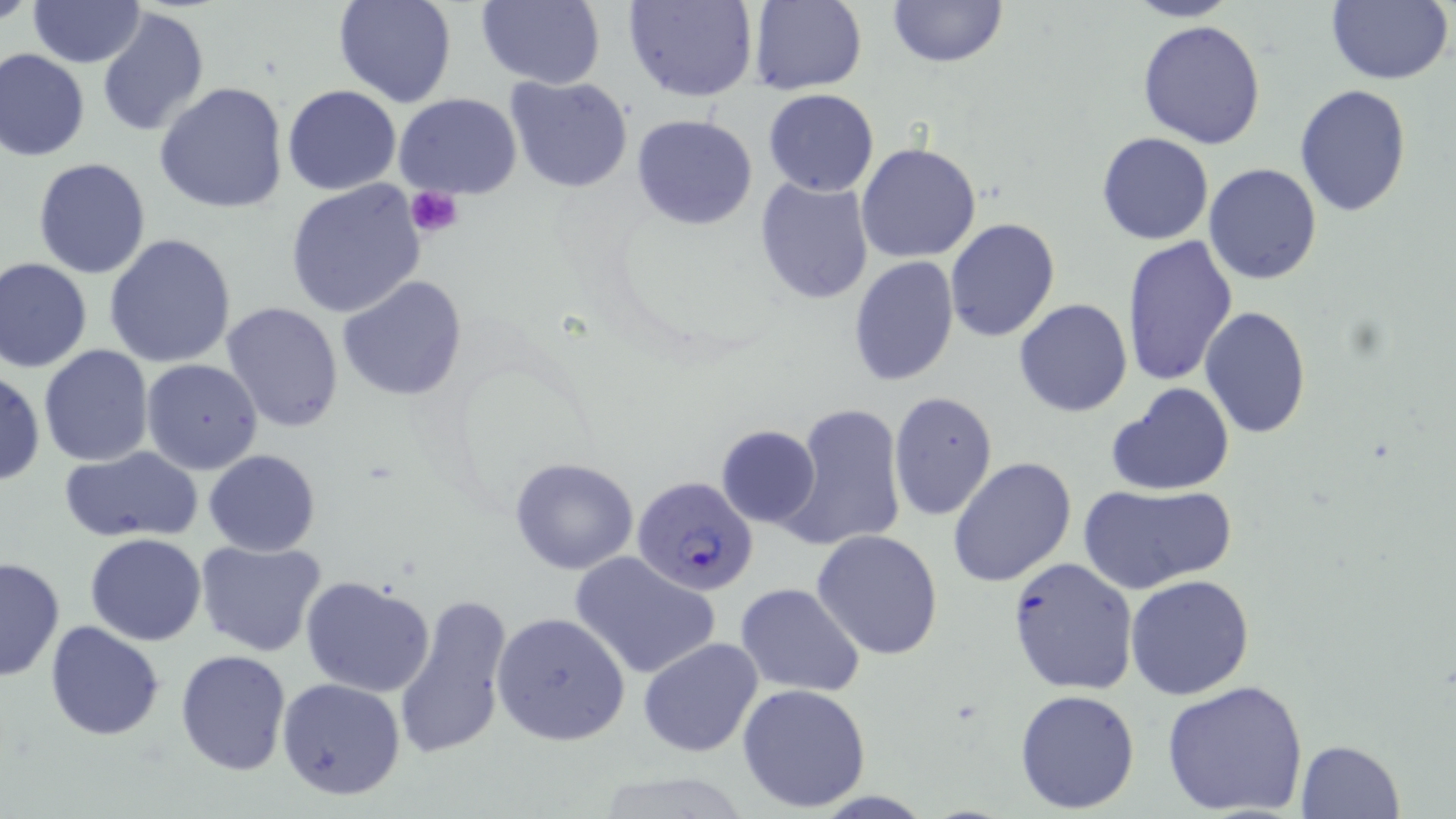

Summary:
  - Coordinate format: approximate bounding boxes as named x1/y1/x2/y2 corners in pixels
  - Plasmodium falciparum-infected red blood cell locations: (x1=633, y1=475, x2=760, y2=595)
  - Uninfected red blood cell locations: (x1=0, y1=0, x2=37, y2=28), (x1=26, y1=0, x2=145, y2=67), (x1=332, y1=0, x2=456, y2=109), (x1=475, y1=0, x2=604, y2=88), (x1=625, y1=0, x2=757, y2=102), (x1=888, y1=0, x2=1006, y2=68), (x1=1123, y1=0, x2=1243, y2=22), (x1=1327, y1=0, x2=1454, y2=85), (x1=750, y1=1, x2=868, y2=95), (x1=97, y1=7, x2=210, y2=138), (x1=1137, y1=19, x2=1268, y2=150), (x1=1, y1=48, x2=90, y2=162), (x1=506, y1=75, x2=633, y2=193), (x1=154, y1=81, x2=290, y2=216), (x1=1295, y1=84, x2=1412, y2=216), (x1=282, y1=85, x2=402, y2=195), (x1=763, y1=89, x2=880, y2=196), (x1=395, y1=93, x2=522, y2=200), (x1=631, y1=112, x2=759, y2=230), (x1=1097, y1=131, x2=1213, y2=245), (x1=855, y1=140, x2=982, y2=263), (x1=33, y1=157, x2=153, y2=279), (x1=1204, y1=163, x2=1321, y2=284), (x1=754, y1=177, x2=873, y2=305), (x1=284, y1=180, x2=428, y2=321), (x1=944, y1=217, x2=1060, y2=342), (x1=103, y1=233, x2=237, y2=369), (x1=1121, y1=233, x2=1238, y2=386), (x1=0, y1=256, x2=93, y2=373), (x1=848, y1=257, x2=960, y2=388), (x1=337, y1=276, x2=467, y2=399), (x1=1014, y1=299, x2=1134, y2=417), (x1=221, y1=301, x2=344, y2=433), (x1=1199, y1=308, x2=1311, y2=438), (x1=39, y1=346, x2=154, y2=466), (x1=141, y1=358, x2=265, y2=475), (x1=0, y1=368, x2=43, y2=489), (x1=1107, y1=383, x2=1236, y2=497), (x1=888, y1=390, x2=997, y2=523), (x1=781, y1=403, x2=905, y2=553), (x1=715, y1=425, x2=821, y2=529), (x1=60, y1=447, x2=204, y2=544), (x1=204, y1=449, x2=320, y2=556), (x1=508, y1=456, x2=638, y2=574), (x1=948, y1=457, x2=1077, y2=589), (x1=1079, y1=483, x2=1235, y2=592), (x1=1019, y1=517, x2=1174, y2=663), (x1=810, y1=529, x2=943, y2=662), (x1=84, y1=533, x2=208, y2=644), (x1=195, y1=539, x2=329, y2=657), (x1=570, y1=550, x2=723, y2=680), (x1=0, y1=555, x2=64, y2=682), (x1=1007, y1=557, x2=1139, y2=696), (x1=1124, y1=574, x2=1254, y2=700), (x1=300, y1=575, x2=437, y2=697), (x1=736, y1=583, x2=865, y2=698), (x1=394, y1=594, x2=513, y2=760), (x1=492, y1=610, x2=631, y2=745), (x1=45, y1=620, x2=164, y2=739), (x1=637, y1=636, x2=765, y2=756), (x1=174, y1=649, x2=291, y2=776), (x1=277, y1=677, x2=407, y2=800), (x1=1163, y1=678, x2=1309, y2=818), (x1=737, y1=683, x2=872, y2=812), (x1=1014, y1=688, x2=1142, y2=814), (x1=1296, y1=739, x2=1406, y2=819)
  - Platelet locations: (x1=406, y1=185, x2=463, y2=238)
  - Slide-level diagnosis: Plasmodium falciparum
  - Magnification: 1000x
  - Modality: optical microscopy
  - Field of view: single
  - Preparation: thin blood film
  - Image size: 1456×819 pixels
  - Stain: May-Grünwald-Giemsa